Classify this cell by malaria status.
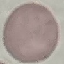
Uninfected.

stain = Giemsa
capture = smartphone through the microscope eyepiece
preparation = thin blood smear
image type = cell patch, automatically extracted from a larger field of view and resized to 64 × 64 pixels